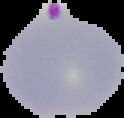
Summary:
  - Malaria status: parasitized
  - Preparation: thin blood film
  - Image size: 124×118 pixels
  - Image type: segmented cell region on a black background